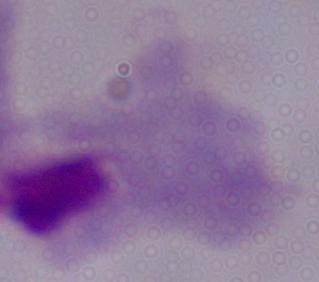

Summary:
  - Identification: trichomonad
  - Magnification: 1000x
  - Modality: photomicrograph